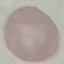
Summary:
  - Result: no malaria parasites detected
  - Image type: automatically extracted cell patch, resized to 64 × 64 pixels
  - Capture: smartphone through the microscope eyepiece
  - Preparation: thin smear
  - Stain: Giemsa